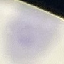
Summary:
  - Result: no malaria parasites detected
  - Capture: smartphone through the microscope eyepiece
  - Stain: Giemsa
  - Image type: cell patch, automatically extracted from a larger field of view and resized to 64 × 64 pixels
  - Preparation: thin blood smear